Classify this cell by malaria status.
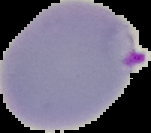
It is parasitized.

Summary:
  - Preparation: thin blood film
  - Image type: segmented cell region with the area outside set to black
  - Image size: 151×133 pixels